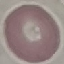

result = no malaria parasites seen
stain = Giemsa
preparation = thin smear
capture = smartphone through the microscope eyepiece
image type = automatically extracted cell patch, resized to 64 × 64 pixels